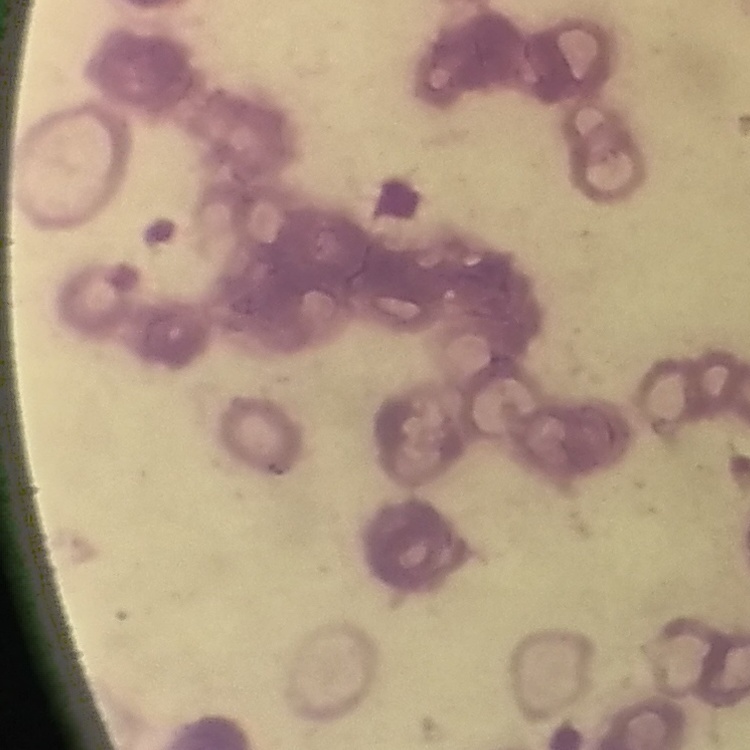
red blood cell morphology = rouleaux formation
image type = one tile cut from a larger photomicrograph
stain = Field's or Giemsa
preparation = thin blood film